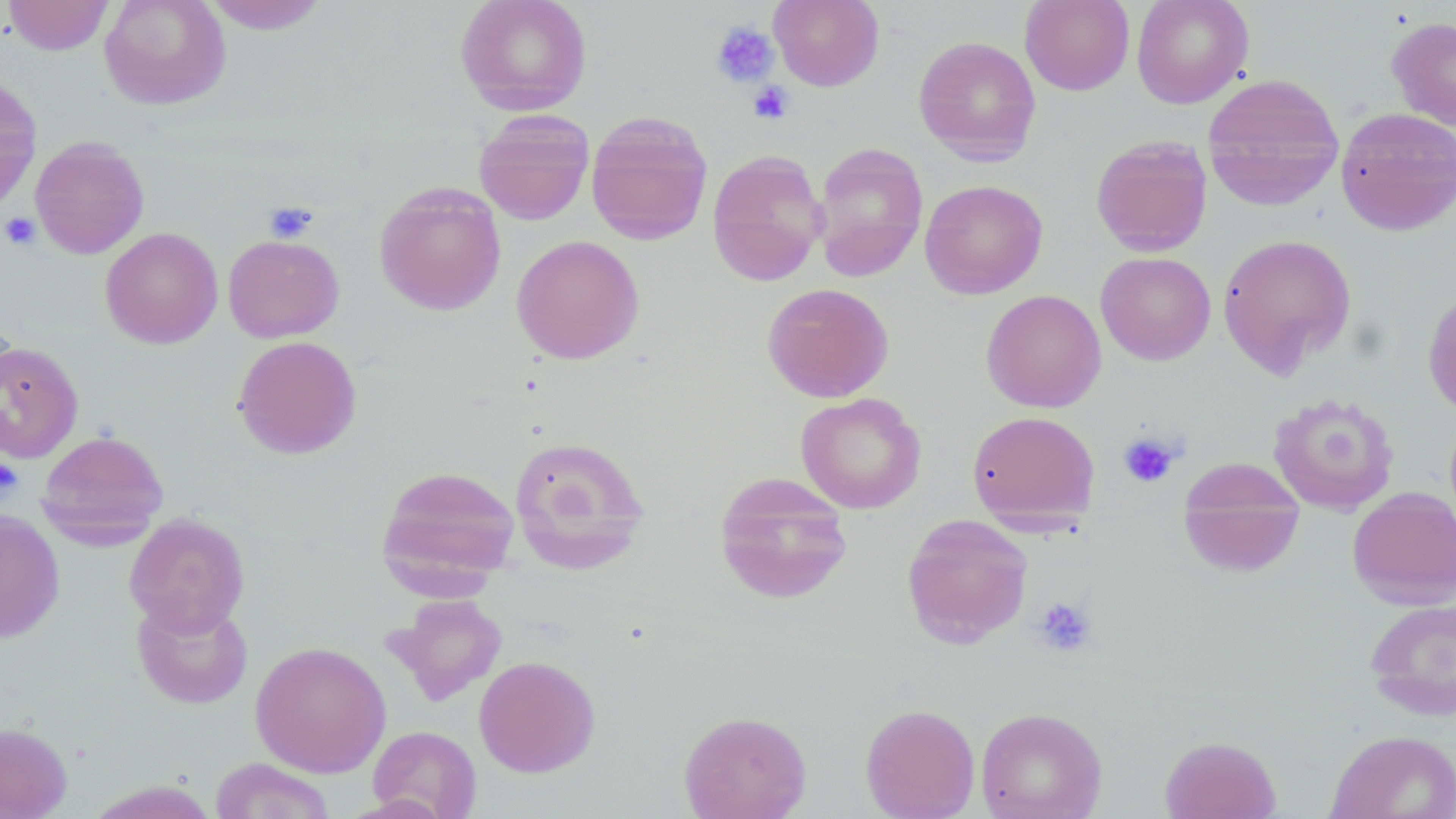

Summary:
  - Coordinate format: approximate bounding boxes as (x1,y1)-(x2,y2) corner pairs in pixels
  - Uninfected red blood cell locations: (4,0)-(113,55), (99,0)-(231,110), (202,0)-(331,34), (454,0)-(593,116), (769,0)-(884,91), (1020,0)-(1135,96), (1131,0)-(1254,108), (1387,16)-(1456,130), (913,35)-(1041,165), (0,73)-(42,213), (1202,73)-(1344,209), (1335,107)-(1456,236), (473,110)-(595,225), (586,111)-(713,245), (1090,135)-(1213,256), (30,136)-(149,259), (812,142)-(928,282), (707,148)-(828,286), (920,179)-(1048,299), (374,182)-(506,316), (100,227)-(223,348), (1217,233)-(1357,377), (223,234)-(344,343), (511,234)-(645,365), (1095,251)-(1216,365), (761,282)-(894,403), (1422,286)-(1456,420), (980,289)-(1107,413), (232,335)-(362,460), (0,340)-(83,463), (795,392)-(926,513), (1268,392)-(1400,515), (966,411)-(1100,528), (37,429)-(169,545), (508,435)-(651,574), (1178,459)-(1305,578), (375,464)-(520,594), (713,472)-(854,605), (1347,487)-(1456,608), (0,510)-(65,643), (124,512)-(251,636), (901,513)-(1033,649), (385,594)-(508,706), (132,595)-(254,709), (1364,597)-(1456,720), (250,640)-(391,777), (474,655)-(601,777), (860,703)-(980,818), (976,707)-(1107,818), (678,710)-(812,819), (0,721)-(72,818), (368,725)-(482,819), (1326,730)-(1456,819), (1160,734)-(1281,819), (211,758)-(335,818), (88,780)-(222,818)
  - Platelet locations: (710,21)-(779,88), (748,81)-(793,124), (263,201)-(320,243), (1,211)-(41,250), (1118,433)-(1180,488), (0,458)-(23,500), (1033,597)-(1097,657)
  - Slide-level diagnosis: negative for blood parasites
  - Modality: optical microscopy
  - Field of view: one of a larger specimen
  - Magnification: 1000x
  - Preparation: thin blood film
  - Image size: 1456×819 pixels
  - Stain: May-Grünwald-Giemsa